Locate platelets.
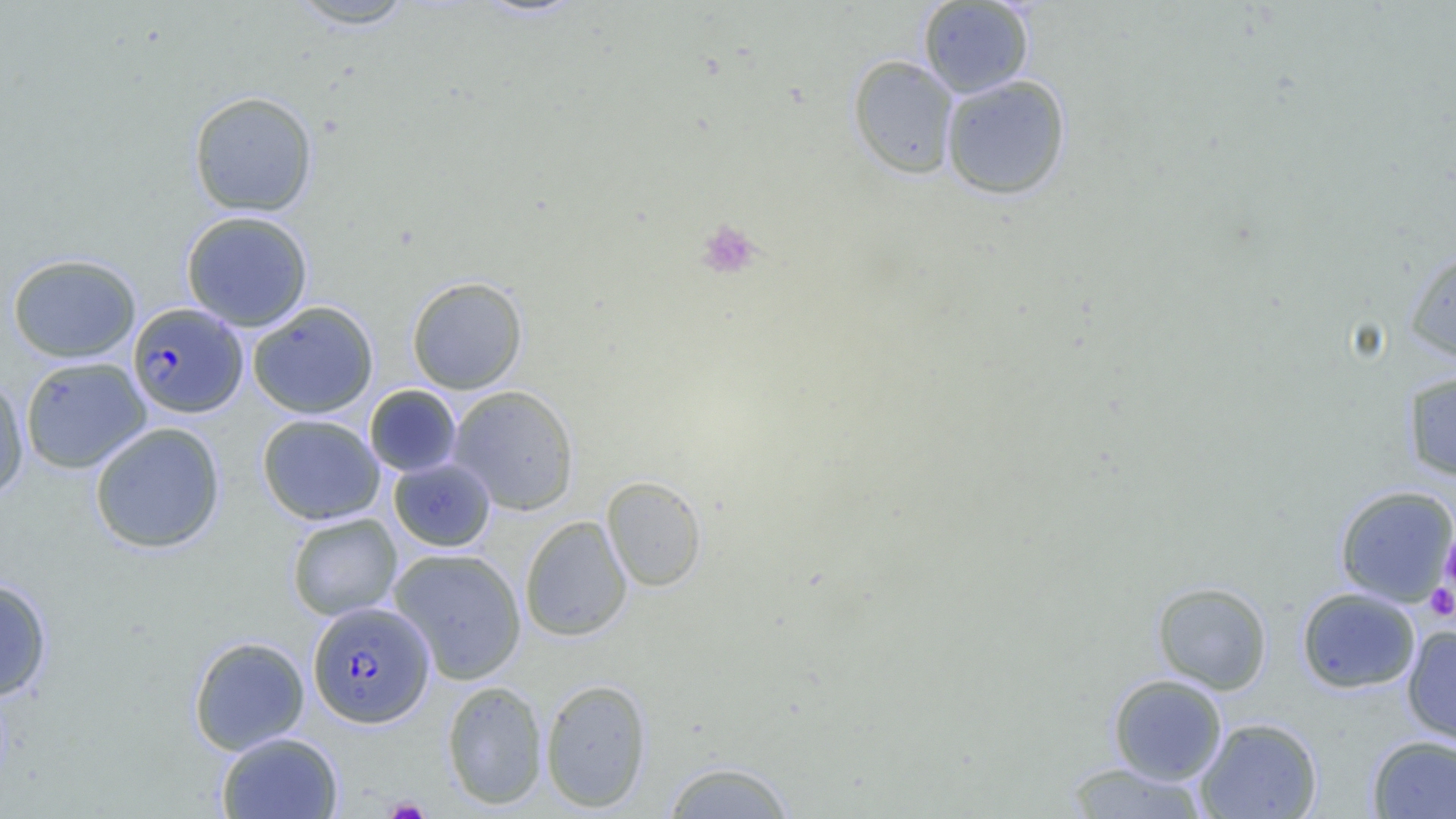

Approximate bounding boxes as named x1/y1/x2/y2 corners in pixels.
Platelets: (x1=695, y1=219, x2=763, y2=279), (x1=1440, y1=527, x2=1456, y2=599), (x1=1425, y1=584, x2=1456, y2=622), (x1=383, y1=797, x2=431, y2=819).

Summary:
  - Uninfected red blood cell locations: (x1=286, y1=1, x2=419, y2=30), (x1=917, y1=1, x2=1035, y2=98), (x1=847, y1=54, x2=959, y2=180), (x1=940, y1=74, x2=1072, y2=201), (x1=189, y1=90, x2=318, y2=217), (x1=181, y1=210, x2=314, y2=332), (x1=1404, y1=247, x2=1456, y2=363), (x1=7, y1=253, x2=141, y2=363), (x1=406, y1=276, x2=528, y2=395), (x1=247, y1=301, x2=379, y2=418), (x1=20, y1=357, x2=151, y2=474), (x1=1402, y1=369, x2=1456, y2=482), (x1=0, y1=377, x2=28, y2=501), (x1=364, y1=385, x2=462, y2=477), (x1=448, y1=385, x2=580, y2=515), (x1=257, y1=414, x2=385, y2=525), (x1=89, y1=422, x2=226, y2=554), (x1=389, y1=457, x2=496, y2=552), (x1=601, y1=475, x2=707, y2=591), (x1=1335, y1=484, x2=1456, y2=607), (x1=286, y1=513, x2=402, y2=621), (x1=519, y1=516, x2=632, y2=642), (x1=388, y1=547, x2=527, y2=685), (x1=0, y1=577, x2=53, y2=701), (x1=1152, y1=581, x2=1272, y2=694), (x1=1296, y1=587, x2=1421, y2=694), (x1=1402, y1=625, x2=1456, y2=746), (x1=189, y1=636, x2=310, y2=754), (x1=1108, y1=673, x2=1227, y2=785), (x1=539, y1=677, x2=653, y2=812), (x1=442, y1=680, x2=548, y2=810), (x1=1195, y1=717, x2=1323, y2=818), (x1=216, y1=731, x2=343, y2=819), (x1=1367, y1=734, x2=1456, y2=818), (x1=661, y1=760, x2=797, y2=818), (x1=1062, y1=761, x2=1210, y2=818)
  - Plasmodium falciparum-infected red blood cell locations: (x1=130, y1=304, x2=251, y2=420), (x1=307, y1=601, x2=435, y2=728)
  - Slide-level diagnosis: Plasmodium falciparum
  - Preparation: thin blood smear
  - Image size: 1456×819 pixels
  - Field of view: single
  - Modality: optical microscopy
  - Magnification: 1000x